State which parasite is depicted.
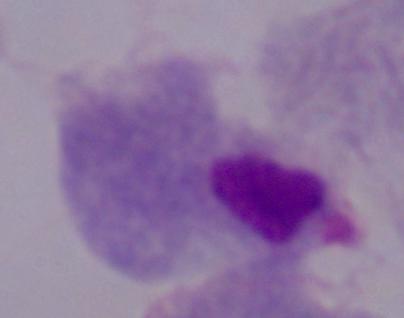
A trichomonad.

Summary:
  - Magnification: 1000x
  - Modality: photomicrograph